Assess this cell for malaria.
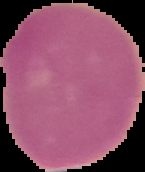

It is uninfected.

image size = 145×172 pixels
image type = segmented cell region on a black background
preparation = thin blood film